Assess this cell for malaria.
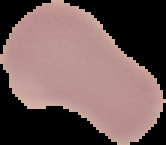

Uninfected.

{
  "image_size": "166×145 pixels",
  "image_type": "segmented cell region on a black background",
  "preparation": "thin blood smear"
}